Report the malaria status of this cell.
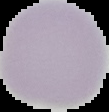

It is uninfected.

Image is 109×112 pixels. From a thin blood smear. The area outside the segmented cell region is set to black.